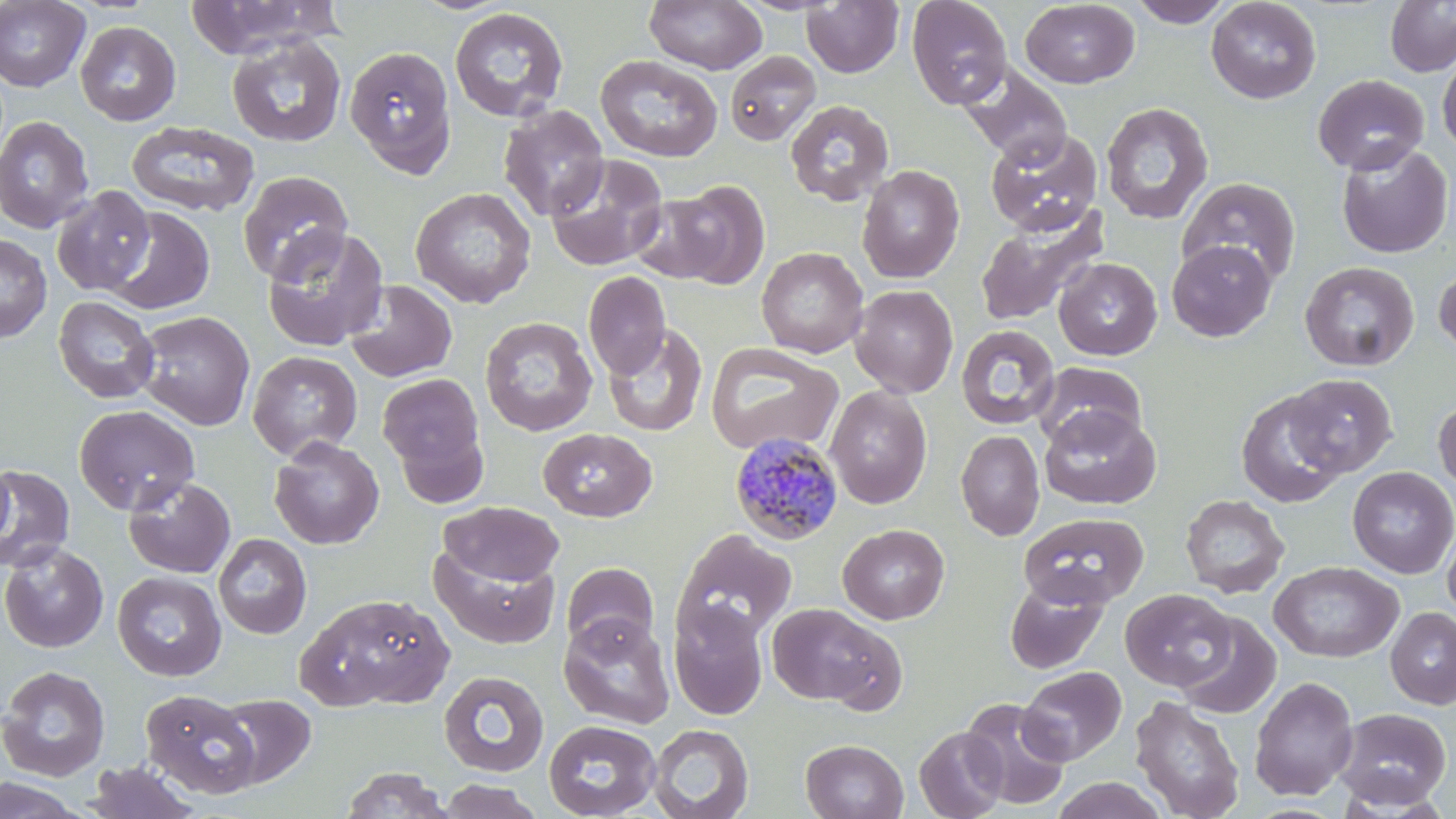
Approximate bounding boxes as (x1, y1, x2, y2) in pixels. Uninfected red blood cell locations: (0, 0, 91, 92), (183, 0, 342, 58), (906, 0, 1013, 109), (1128, 0, 1235, 27), (1206, 0, 1321, 104), (644, 1, 767, 74), (802, 1, 904, 78), (1020, 1, 1140, 88), (1385, 1, 1456, 77), (449, 7, 569, 122), (76, 21, 181, 126), (226, 35, 347, 148), (344, 44, 457, 177), (725, 51, 821, 145), (1437, 52, 1456, 157), (595, 55, 723, 162), (958, 64, 1073, 164), (1312, 73, 1429, 175), (785, 99, 894, 207), (1100, 103, 1213, 225), (498, 104, 609, 223), (0, 115, 95, 233), (126, 121, 259, 217), (984, 128, 1104, 236), (1335, 142, 1454, 259), (544, 154, 668, 272), (857, 165, 965, 283), (238, 170, 353, 284), (1177, 176, 1301, 287), (659, 180, 771, 289), (51, 186, 155, 296), (410, 187, 536, 308), (102, 206, 215, 315), (974, 206, 1110, 327), (262, 226, 389, 351), (0, 233, 51, 342), (1167, 239, 1277, 342), (756, 247, 869, 358), (1053, 257, 1162, 360), (1300, 261, 1419, 371), (1434, 262, 1456, 360), (583, 271, 670, 380), (344, 280, 458, 383), (850, 285, 959, 398), (53, 296, 159, 404), (134, 311, 255, 431), (480, 316, 597, 436), (603, 324, 707, 437), (955, 325, 1059, 429), (705, 342, 843, 456), (247, 350, 363, 461), (1033, 361, 1147, 450), (377, 373, 487, 483), (1284, 373, 1398, 477), (824, 385, 932, 508), (1236, 389, 1347, 508), (1433, 398, 1456, 494), (74, 404, 199, 515), (1038, 405, 1161, 510), (538, 427, 657, 522), (956, 429, 1045, 541), (269, 436, 384, 549), (0, 462, 14, 555), (0, 464, 75, 574), (1348, 466, 1456, 578), (123, 476, 236, 578), (1180, 494, 1289, 598), (439, 501, 564, 586), (1019, 512, 1149, 609), (1441, 523, 1456, 624), (838, 524, 949, 624), (672, 529, 796, 647), (213, 533, 312, 640), (0, 543, 108, 653), (430, 544, 560, 649), (561, 561, 659, 655), (1270, 561, 1403, 663), (112, 571, 227, 681), (1004, 578, 1108, 675), (1121, 589, 1235, 691), (297, 592, 453, 712), (668, 601, 768, 720), (766, 603, 894, 707), (1386, 607, 1456, 709), (1175, 612, 1281, 719), (558, 613, 676, 730), (0, 664, 111, 782), (1018, 665, 1127, 765), (439, 671, 549, 777), (1249, 676, 1358, 800), (140, 689, 261, 798), (215, 694, 315, 788), (1129, 696, 1245, 819), (961, 698, 1071, 810), (1332, 707, 1452, 810), (543, 719, 661, 819), (648, 724, 754, 819), (914, 727, 1008, 818), (801, 739, 908, 819), (86, 761, 200, 818), (341, 767, 452, 818), (0, 775, 90, 818), (1051, 776, 1168, 819), (436, 779, 544, 819). Plasmodium malariae-infected red blood cell locations: (729, 431, 844, 546). Slide-level diagnosis: Plasmodium malariae. Optical microscopy. 1000x magnification. May-Grünwald-Giemsa-stained preparation. Single field of view. Image is 1456×819 pixels. Thin blood film.